Assess for parasitized red blood cells.
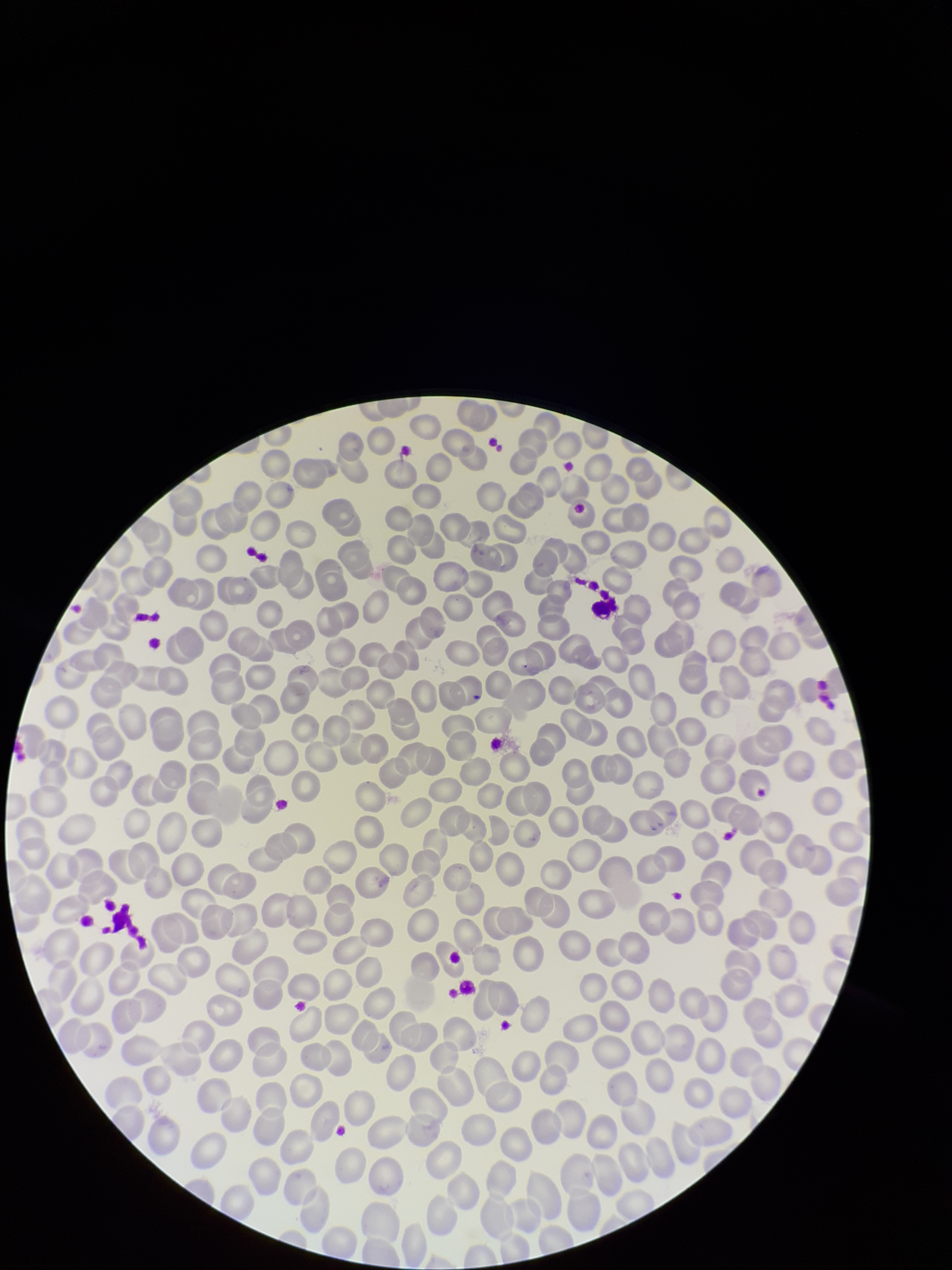
None seen.

Parasitized red blood cell count: 0. Single field of view. Preparation: thin smear. Patient malaria status: negative. Smartphone photograph taken through the eyepiece of a microscope. Red blood cell count: 224. Stained with Giemsa. Image is 952×1270 pixels.